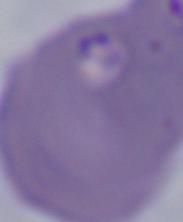

magnification = 1000x
identification = Babesia
modality = photomicrograph